Assess this cell for malaria.
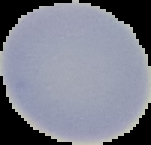

It is uninfected.

{
  "preparation": "thin blood smear",
  "image_type": "segmented cell region with the area outside set to black",
  "image_size": "151×145 pixels"
}